Name the parasite shown.
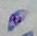

This is Toxoplasma gondii.

Micrograph. 1000x magnification.